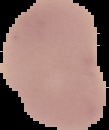
image type = segmented cell region with the area outside set to black
image size = 109×130 pixels
malaria status = uninfected
preparation = thin blood smear